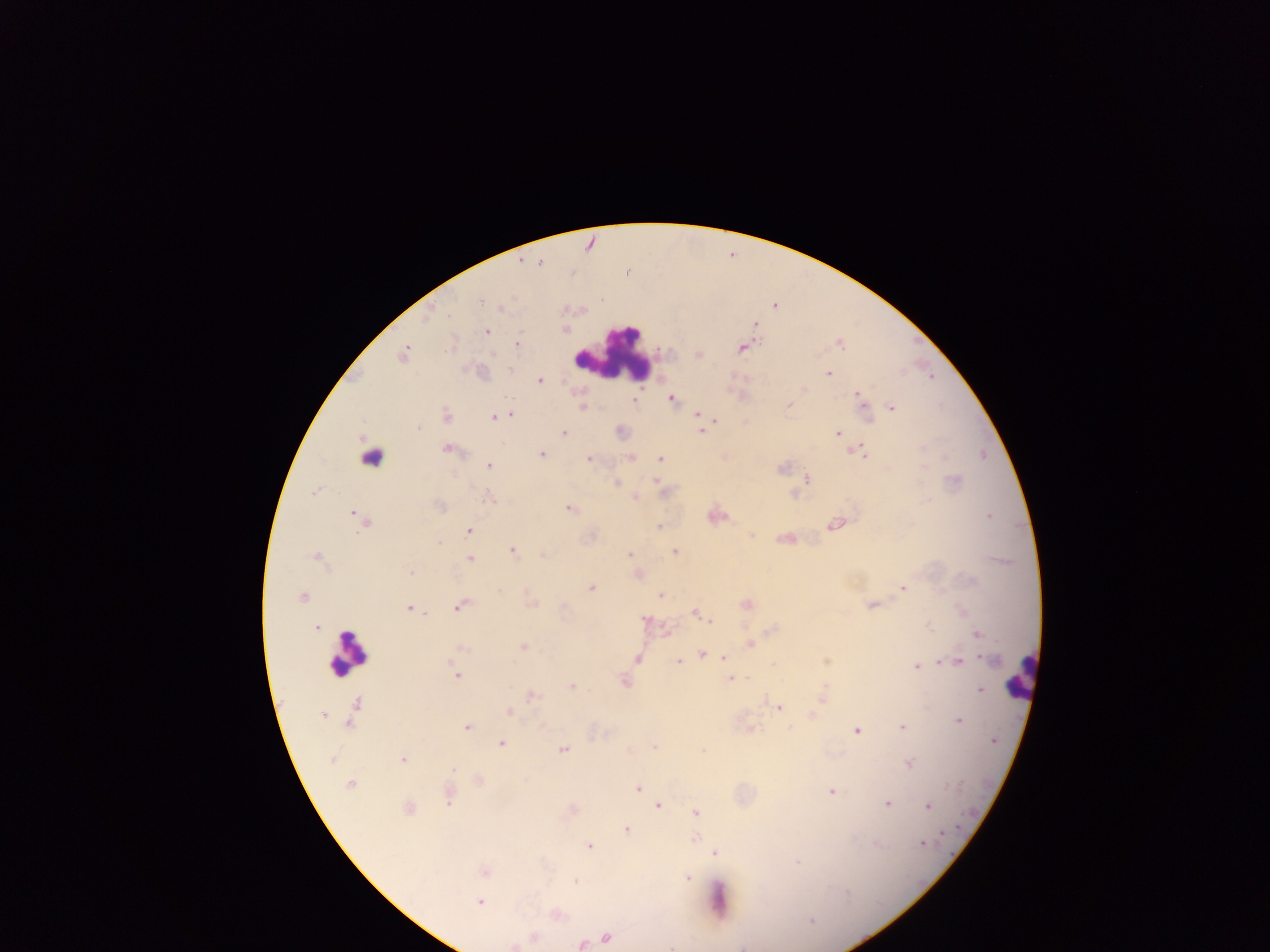
Approximate centers as x y in pixels. Leukocyte locations: 608 351; 349 653; 1019 675. Plasmodium parasite locations: 540 264; 511 297; 479 301; 600 302; 775 307; 428 320; 565 328; 487 330; 518 343; 837 344; 742 349; 404 352; 494 353; 402 357; 830 375; 540 379; 804 389; 858 394; 671 398; 861 400; 582 407; 789 407; 894 407; 511 413; 696 414; 447 417; 495 418; 718 420; 418 427; 701 432; 564 433; 837 434; 446 449; 861 451; 542 454; 590 457; 630 457; 660 457; 488 466; 806 479; 656 481; 616 484; 796 496; 634 498; 489 499; 438 504; 567 507; 353 514; 988 516; 834 523; 659 527; 361 530; 468 531; 439 543; 675 551; 513 552; 629 552; 543 554; 470 559; 408 572; 638 574; 592 589; 902 589; 659 594; 531 604; 871 605; 408 608; 456 608; 695 613; 701 615; 646 621; 709 621; 316 626; 977 634; 522 645; 460 648; 983 654; 702 655; 638 657; 724 658; 826 660; 449 661; 678 661; 958 661; 773 665; 915 665; 456 676; 733 679; 625 680; 573 686; 978 689; 530 694; 822 698; 781 708; 510 712; 813 715; 323 716; 959 722; 466 726; 542 726; 788 726; 901 726; 752 728; 856 733; 993 740; 501 743; 655 746; 703 750; 564 751; 402 759; 454 768; 638 788; 831 790; 448 801; 886 804; 658 805; 927 805; 696 813; 627 830; 696 837; 923 845; 591 846; 716 852; 799 862; 484 871; 688 877; 577 881; 480 901; 811 921. Collected in Ghana. One field of view. Photographed through a microscope with a mobile-phone camera. Thick blood film. Image is 1270×952 pixels.